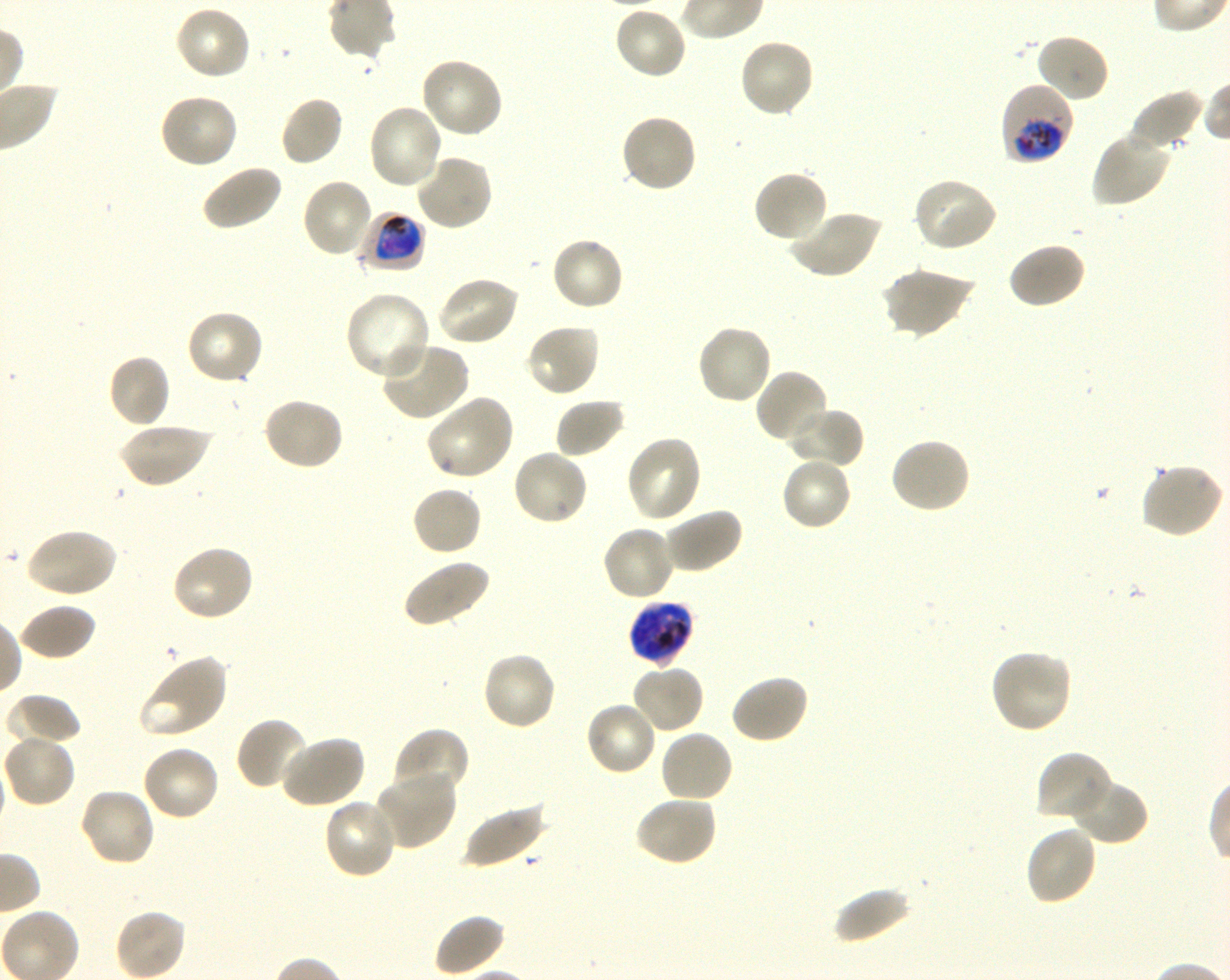
Approximate bounding boxes as (x1, y1, x2, y2) in pixels. Not every red blood cell is marked. A life-cycle stage — or a range of stages, where the recorded stages span more than one — follows each staged infected red blood cell.
Summary:
  - Locations of uninfected red blood cells: (173, 4, 252, 81), (613, 5, 688, 80), (1035, 33, 1111, 104), (738, 38, 816, 119), (420, 56, 505, 139), (1130, 89, 1206, 152), (158, 93, 240, 170), (279, 95, 344, 167), (367, 103, 445, 190), (620, 112, 699, 194), (1091, 129, 1171, 208), (413, 153, 495, 231), (199, 164, 282, 232), (752, 169, 828, 245), (300, 177, 374, 259), (911, 177, 998, 253), (788, 209, 882, 280), (550, 235, 625, 313), (1007, 241, 1087, 310), (880, 267, 973, 340), (435, 275, 521, 347), (344, 291, 432, 381), (185, 309, 265, 386), (524, 323, 601, 398), (696, 323, 773, 406), (379, 341, 470, 421), (107, 353, 172, 428), (755, 369, 830, 446), (425, 394, 515, 482), (262, 396, 345, 472), (554, 397, 628, 459), (784, 406, 864, 469), (118, 422, 211, 489), (624, 434, 702, 524), (889, 435, 972, 514), (510, 447, 590, 526), (779, 456, 854, 532), (1140, 463, 1225, 539), (410, 485, 483, 557), (660, 507, 743, 575), (601, 524, 677, 602), (26, 527, 118, 599), (170, 543, 255, 623), (401, 558, 491, 629), (17, 604, 96, 662), (989, 647, 1074, 734), (481, 651, 557, 732), (139, 653, 229, 739), (631, 663, 706, 735), (729, 674, 809, 745), (5, 693, 82, 748), (584, 701, 658, 777), (235, 716, 312, 792), (393, 728, 469, 803), (658, 729, 734, 805), (2, 732, 76, 808), (278, 735, 366, 809), (141, 743, 222, 822), (1036, 751, 1113, 824), (373, 769, 458, 849), (1070, 777, 1149, 846), (78, 787, 156, 867), (634, 794, 718, 866), (322, 797, 398, 880), (461, 800, 547, 869), (1024, 825, 1099, 906), (832, 885, 912, 945), (114, 907, 191, 980), (432, 914, 505, 977)
  - Locations of infected red blood cells: (999, 82, 1075, 165) trophozoite; (359, 211, 426, 272) early trophozoite to early schizont; (628, 600, 694, 666) late trophozoite to late schizont
  - Donor blood group: O+
  - Culture: in-vitro Plasmodium falciparum strain 3D7, shaking
  - Preparation: thin blood film
  - Field of view: single
  - Stain: Giemsa
  - Objective: 100x, oil immersion, numerical aperture 1.30
  - Image size: 1230×980 pixels